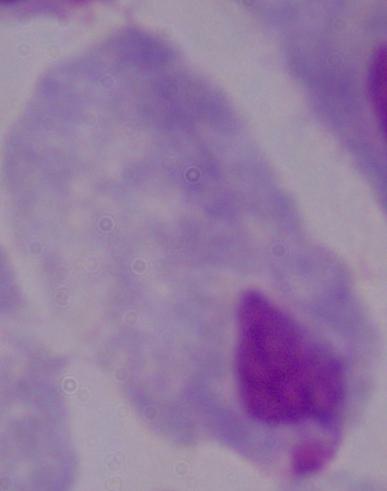
Summary:
  - Modality: micrograph
  - Identification: trichomonad
  - Magnification: 1000x